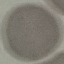 Malaria status: uninfected. Giemsa stain. Cell patch, automatically extracted from a larger field of view and resized to 64 × 64 pixels. Thin blood smear. Acquired by smartphone through the microscope eyepiece.